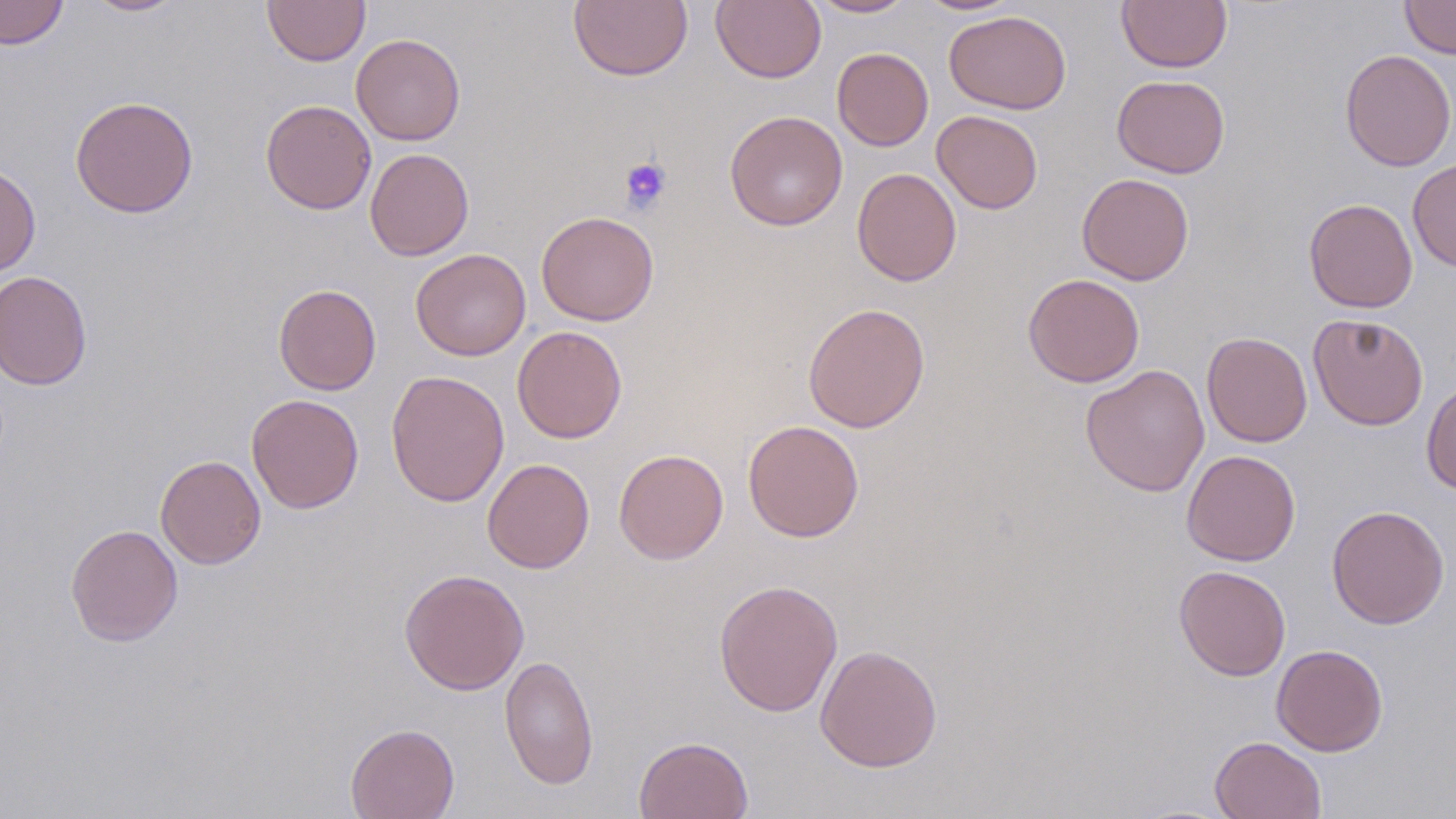
Summary:
  - Coordinate format: approximate bounding boxes as [x1, y1, x2, y2] in pixels
  - Platelet locations: [618, 157, 672, 215]
  - Uninfected red blood cell locations: [0, 0, 68, 50], [82, 0, 188, 17], [262, 0, 370, 67], [711, 0, 826, 84], [806, 0, 917, 18], [914, 0, 1023, 15], [1117, 0, 1231, 73], [1400, 0, 1456, 59], [568, 1, 693, 82], [944, 10, 1071, 114], [351, 33, 466, 145], [832, 47, 933, 152], [1339, 49, 1456, 172], [1112, 74, 1230, 178], [70, 95, 199, 218], [260, 99, 376, 214], [932, 109, 1043, 214], [724, 110, 848, 231], [364, 148, 474, 261], [1407, 159, 1456, 271], [0, 164, 41, 276], [852, 168, 962, 286], [1077, 173, 1194, 285], [1303, 197, 1418, 313], [536, 211, 659, 326], [410, 248, 531, 361], [0, 270, 92, 390], [1023, 273, 1145, 388], [273, 284, 382, 395], [803, 302, 930, 433], [1308, 313, 1429, 431], [512, 325, 628, 443], [1202, 331, 1313, 447], [1080, 364, 1209, 497], [386, 369, 509, 508], [1421, 381, 1456, 495], [246, 394, 364, 514], [743, 420, 864, 542], [613, 448, 729, 564], [1181, 449, 1301, 566], [155, 454, 266, 569], [483, 458, 594, 573], [1326, 504, 1450, 629], [65, 523, 183, 647], [1173, 564, 1291, 681], [399, 568, 529, 695], [713, 579, 843, 717], [815, 644, 943, 773], [1271, 644, 1388, 757], [499, 655, 599, 790], [345, 723, 460, 819], [634, 735, 754, 819], [1210, 735, 1326, 819]
  - Slide-level diagnosis: no evidence of blood parasites
  - Image size: 1456×819 pixels
  - Stain: May-Grünwald-Giemsa
  - Modality: light microscopy
  - Preparation: thin blood smear
  - Magnification: 1000x
  - Field of view: single